Classify this cell by malaria status.
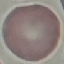
It is uninfected.

Summary:
  - Stain: Giemsa
  - Preparation: thin blood film
  - Capture: smartphone through the microscope eyepiece
  - Image type: automatically extracted cell patch, resized to 64 × 64 pixels